Assess this cell for malaria.
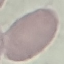
It is uninfected.

Automatically extracted cell patch, resized to 64 × 64 pixels. Thin blood smear. Giemsa-stained preparation. Acquired by smartphone through the microscope eyepiece.